Identify the cell.
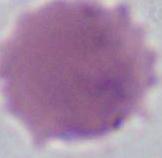
An erythrocyte.

Captured at 1000x magnification. Photomicrograph.